Give the extent of all Plasmodium falciparum-infected red blood cells.
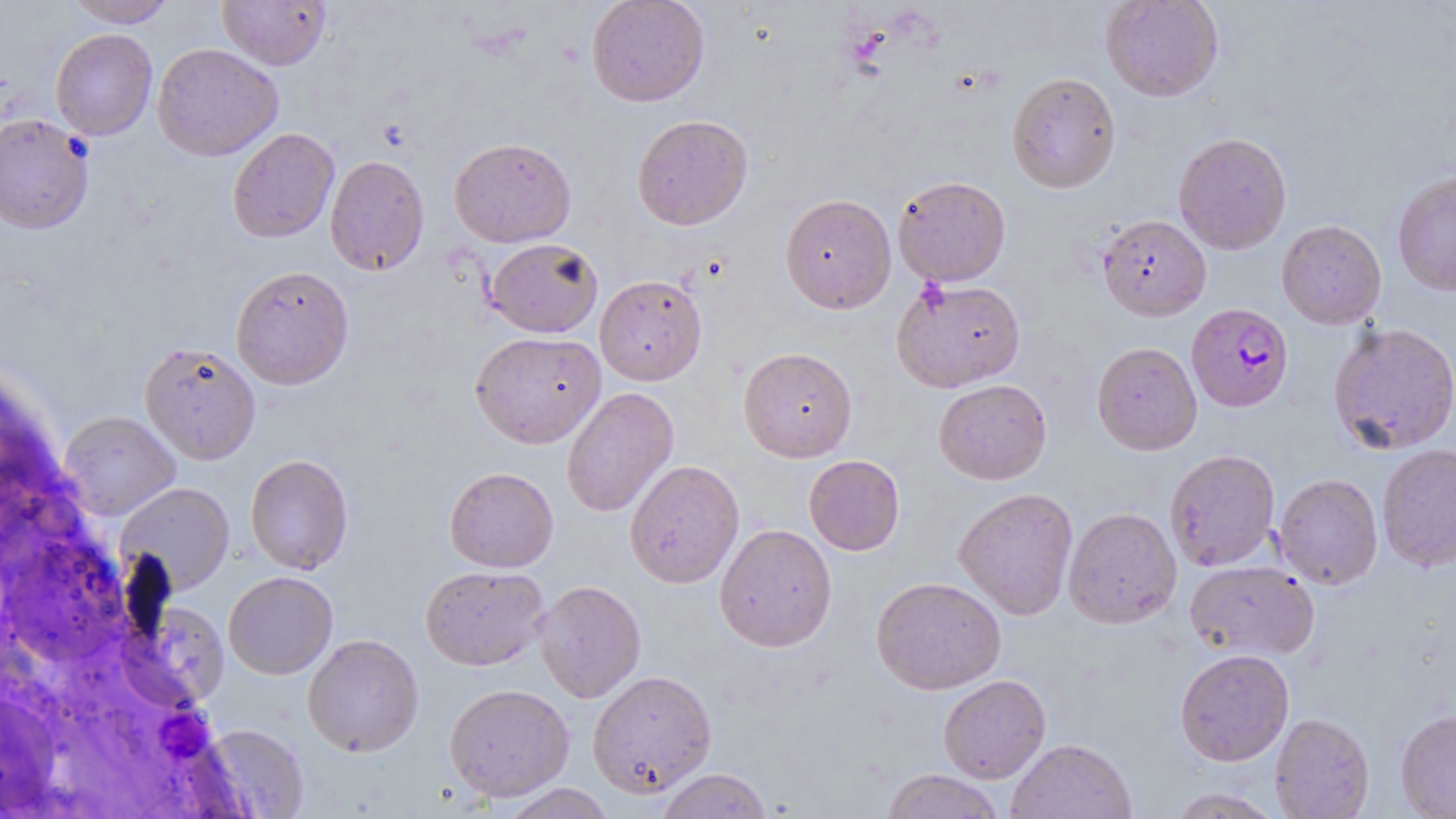
Approximate bounding boxes as named x1/y1/x2/y2 corners in pixels.
Plasmodium falciparum-infected red blood cells: (x1=1187, y1=303, x2=1293, y2=412).

Uninfected red blood cell locations: (x1=64, y1=0, x2=177, y2=27), (x1=217, y1=0, x2=332, y2=70), (x1=586, y1=0, x2=710, y2=107), (x1=1100, y1=0, x2=1223, y2=102), (x1=51, y1=28, x2=157, y2=140), (x1=152, y1=42, x2=283, y2=161), (x1=1007, y1=72, x2=1120, y2=193), (x1=0, y1=112, x2=94, y2=234), (x1=632, y1=114, x2=752, y2=230), (x1=227, y1=127, x2=339, y2=243), (x1=1173, y1=132, x2=1292, y2=254), (x1=449, y1=137, x2=576, y2=247), (x1=325, y1=154, x2=430, y2=275), (x1=1392, y1=172, x2=1456, y2=296), (x1=893, y1=175, x2=1010, y2=286), (x1=780, y1=193, x2=896, y2=314), (x1=1097, y1=215, x2=1211, y2=321), (x1=1277, y1=220, x2=1387, y2=329), (x1=485, y1=237, x2=603, y2=338), (x1=230, y1=264, x2=354, y2=389), (x1=595, y1=274, x2=707, y2=385), (x1=891, y1=277, x2=1025, y2=392), (x1=1328, y1=323, x2=1456, y2=455), (x1=470, y1=331, x2=605, y2=448), (x1=139, y1=342, x2=261, y2=464), (x1=1092, y1=342, x2=1202, y2=455), (x1=738, y1=347, x2=857, y2=462), (x1=934, y1=379, x2=1052, y2=484), (x1=562, y1=387, x2=679, y2=517), (x1=59, y1=411, x2=180, y2=520), (x1=1377, y1=444, x2=1456, y2=572), (x1=1165, y1=449, x2=1280, y2=571), (x1=244, y1=454, x2=353, y2=575), (x1=804, y1=455, x2=905, y2=555), (x1=624, y1=459, x2=744, y2=588), (x1=444, y1=467, x2=559, y2=572), (x1=1274, y1=474, x2=1383, y2=590), (x1=116, y1=482, x2=235, y2=595), (x1=954, y1=487, x2=1078, y2=620), (x1=1064, y1=507, x2=1182, y2=628), (x1=715, y1=523, x2=837, y2=652), (x1=1185, y1=561, x2=1321, y2=660), (x1=420, y1=565, x2=549, y2=671), (x1=224, y1=571, x2=338, y2=679), (x1=871, y1=576, x2=1006, y2=695), (x1=534, y1=580, x2=646, y2=703), (x1=115, y1=603, x2=231, y2=715), (x1=303, y1=633, x2=424, y2=757), (x1=1175, y1=649, x2=1294, y2=766), (x1=587, y1=670, x2=717, y2=797), (x1=938, y1=674, x2=1051, y2=783), (x1=444, y1=683, x2=574, y2=802), (x1=1396, y1=709, x2=1456, y2=818), (x1=1270, y1=713, x2=1374, y2=818), (x1=199, y1=723, x2=310, y2=818), (x1=1007, y1=738, x2=1137, y2=819), (x1=655, y1=768, x2=773, y2=819), (x1=880, y1=769, x2=1005, y2=819), (x1=500, y1=783, x2=616, y2=818), (x1=1165, y1=787, x2=1285, y2=818). Slide-level diagnosis: Plasmodium falciparum. 1000x magnification. May-Grünwald-Giemsa stain. Optical microscopy. Image is 1456×819 pixels. Thin blood film. Single field of view.